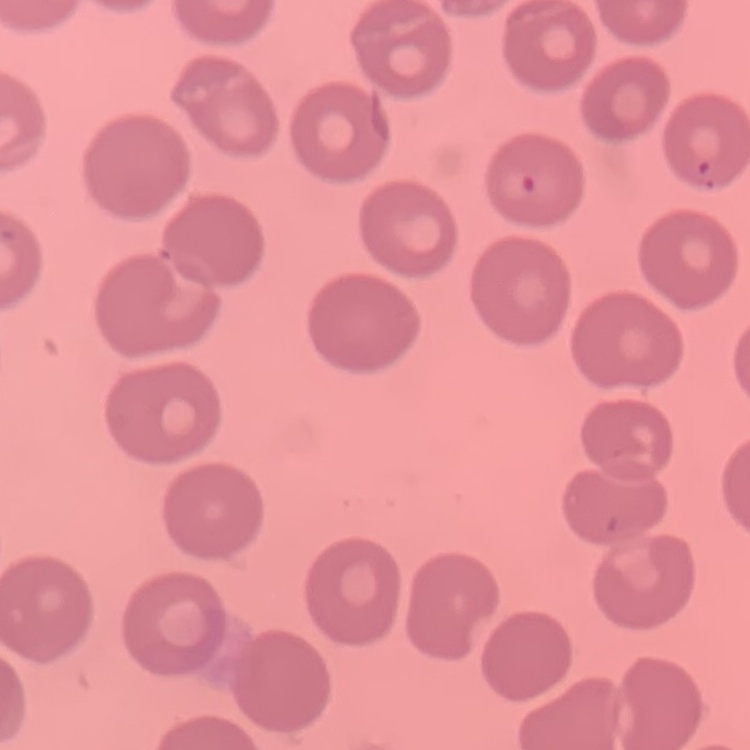
The erythrocytes exhibit no rouleaux formation. One tile cut from a larger photomicrograph. Thin blood film. Stained with either Field's or Giemsa.